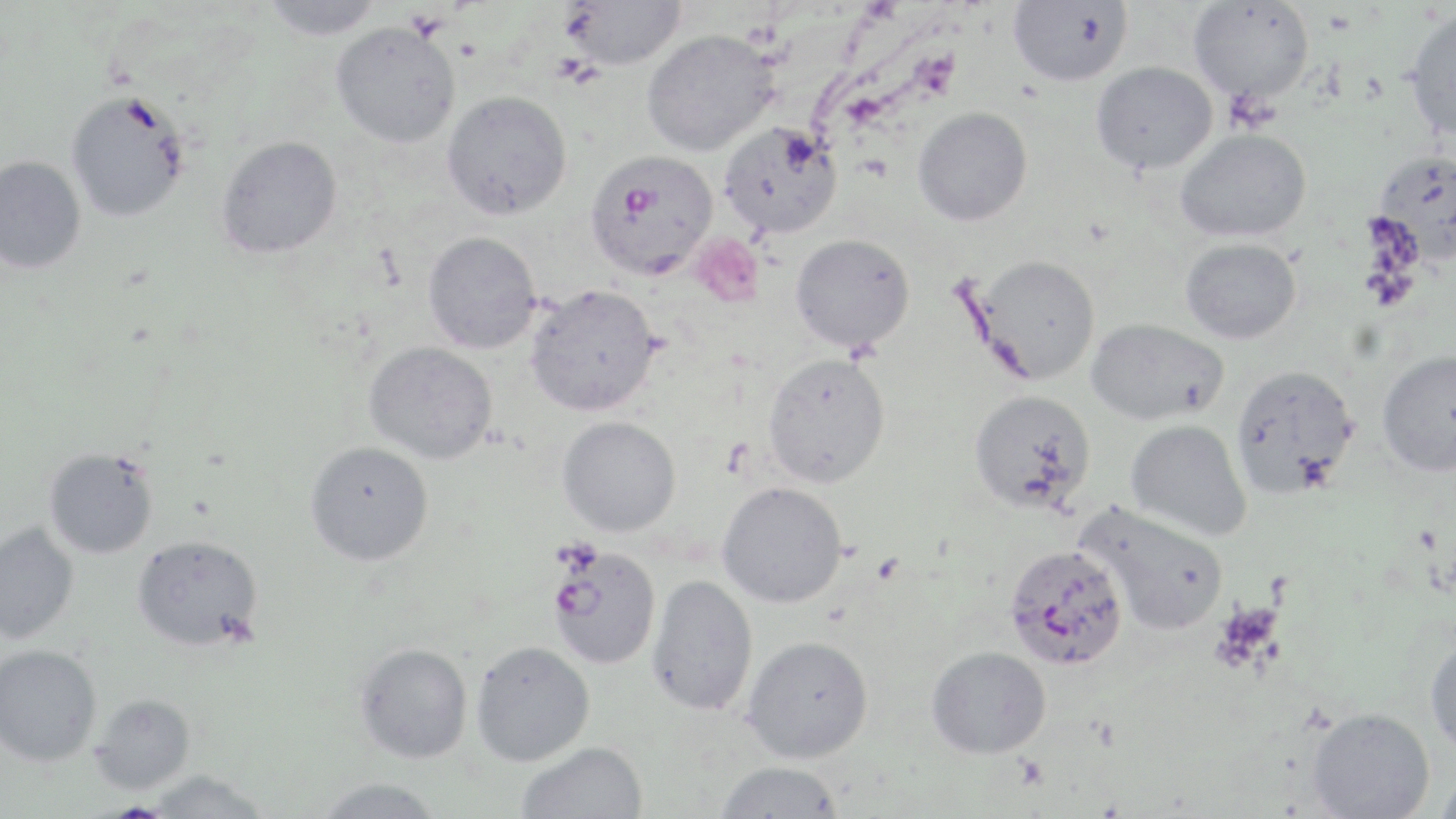

slide-level diagnosis = Plasmodium falciparum
magnification = 1000x
uninfected red blood cell locations = approximate bounding boxes as named x1/y1/x2/y2 corners in pixels: (x1=561, y1=0, x2=688, y2=70), (x1=1188, y1=0, x2=1314, y2=103), (x1=261, y1=1, x2=384, y2=40), (x1=1008, y1=1, x2=1132, y2=86), (x1=1403, y1=8, x2=1456, y2=141), (x1=331, y1=21, x2=461, y2=149), (x1=642, y1=29, x2=779, y2=156), (x1=1092, y1=62, x2=1218, y2=174), (x1=65, y1=88, x2=192, y2=223), (x1=441, y1=90, x2=572, y2=221), (x1=913, y1=107, x2=1032, y2=226), (x1=719, y1=121, x2=843, y2=239), (x1=1175, y1=128, x2=1311, y2=242), (x1=216, y1=135, x2=343, y2=260), (x1=1373, y1=149, x2=1456, y2=262), (x1=0, y1=155, x2=86, y2=274), (x1=423, y1=231, x2=541, y2=353), (x1=790, y1=233, x2=915, y2=353), (x1=1180, y1=238, x2=1302, y2=344), (x1=967, y1=255, x2=1102, y2=385), (x1=525, y1=284, x2=662, y2=416), (x1=1086, y1=318, x2=1229, y2=425), (x1=364, y1=341, x2=498, y2=465), (x1=1376, y1=350, x2=1456, y2=477), (x1=762, y1=351, x2=890, y2=487), (x1=1230, y1=363, x2=1359, y2=498), (x1=968, y1=389, x2=1096, y2=513), (x1=557, y1=415, x2=681, y2=537), (x1=1125, y1=420, x2=1252, y2=542), (x1=305, y1=441, x2=434, y2=566), (x1=44, y1=447, x2=159, y2=559), (x1=717, y1=481, x2=848, y2=608), (x1=1077, y1=502, x2=1229, y2=636), (x1=0, y1=521, x2=80, y2=644), (x1=131, y1=534, x2=264, y2=651), (x1=646, y1=574, x2=758, y2=717), (x1=742, y1=635, x2=874, y2=763), (x1=1425, y1=635, x2=1456, y2=757), (x1=471, y1=641, x2=595, y2=766), (x1=354, y1=642, x2=473, y2=763), (x1=0, y1=644, x2=102, y2=766), (x1=926, y1=646, x2=1052, y2=759), (x1=90, y1=693, x2=196, y2=793), (x1=1307, y1=707, x2=1435, y2=819), (x1=516, y1=741, x2=649, y2=819), (x1=714, y1=761, x2=844, y2=818), (x1=144, y1=770, x2=272, y2=818), (x1=1435, y1=771, x2=1456, y2=818), (x1=312, y1=777, x2=446, y2=819)
image size = 1456×819 pixels
field of view = one of a larger specimen
platelet locations = approximate bounding boxes as named x1/y1/x2/y2 corners in pixels: (x1=691, y1=234, x2=764, y2=309), (x1=1012, y1=755, x2=1050, y2=790)
modality = light microscopy
Plasmodium falciparum-infected red blood cell locations = approximate bounding boxes as named x1/y1/x2/y2 corners in pixels: (x1=584, y1=150, x2=718, y2=280), (x1=1002, y1=543, x2=1129, y2=671), (x1=546, y1=545, x2=661, y2=669)
stain = May-Grünwald-Giemsa
preparation = thin blood smear